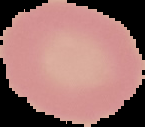
Summary:
  - Preparation: thin blood smear
  - Image size: 145×127 pixels
  - Malaria status: uninfected
  - Image type: segmented cell region on a black background